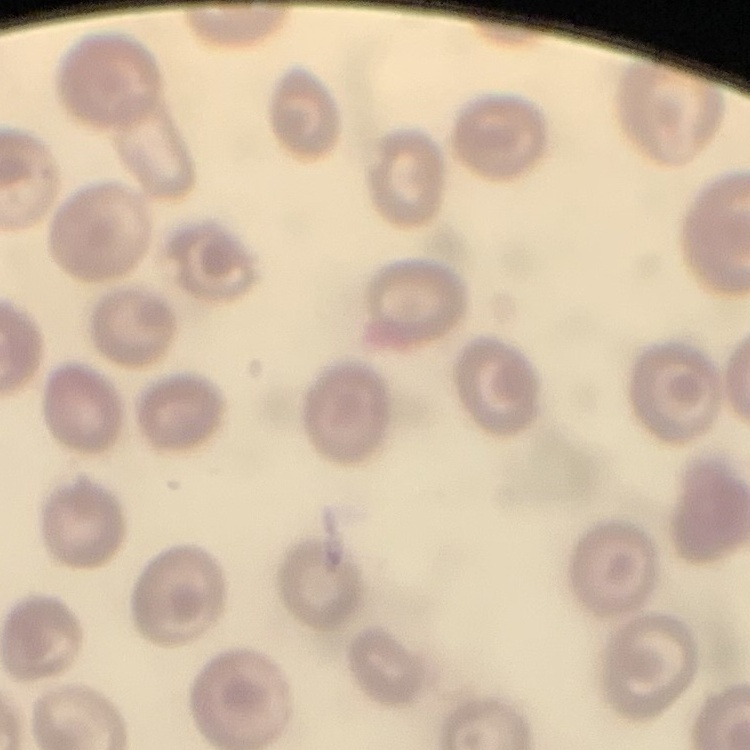 The red blood cells exhibit no rouleaux formation. Thin blood smear. One tile cut from a larger photomicrograph. Stained with either Field's or Giemsa.